Report the malaria status.
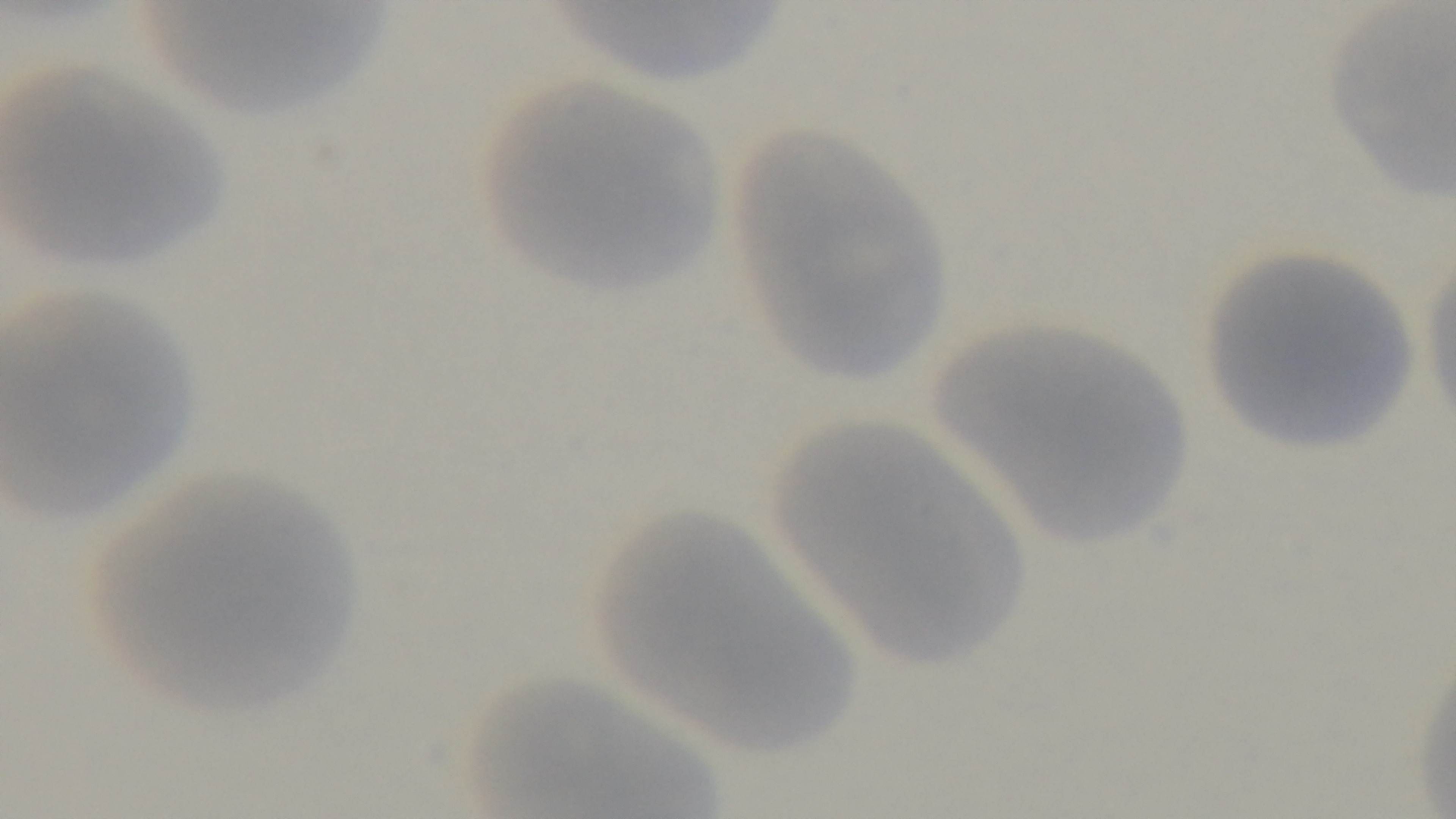

Uninfected.

Preparation: thin. Light microscopy. Giemsa stain. Mounted 4K digital camera. 100x oil-immersion objective. One field from the slide.